Outline each Babesia divergens-infected red blood cell.
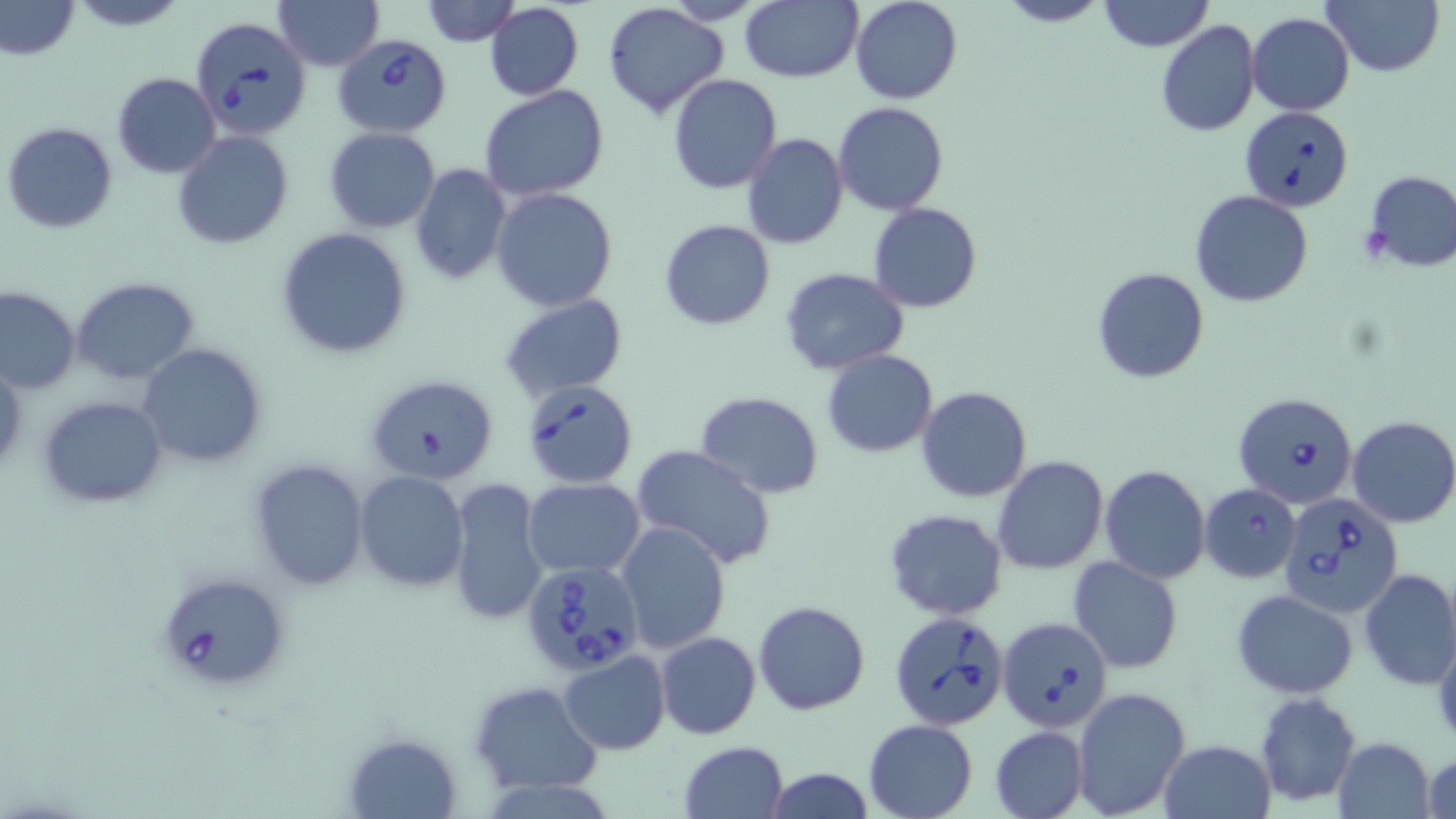

Approximate bounding boxes as [x1, y1, x2, y2] in pixels.
Babesia divergens-infected red blood cells: [189, 16, 312, 140], [333, 36, 454, 137], [1241, 105, 1354, 211], [519, 379, 640, 489], [1234, 392, 1359, 509], [1280, 490, 1404, 616], [520, 561, 645, 678], [154, 570, 292, 690], [889, 608, 1009, 727], [996, 615, 1112, 731].

slide-level diagnosis = Babesia divergens
magnification = 1000x
preparation = thin blood film
stain = May-Grünwald-Giemsa
modality = light microscopy
field of view = single
uninfected red blood cell locations = approximate bounding boxes as [x1, y1, x2, y2] in pixels: [2, 0, 78, 60], [67, 0, 187, 30], [272, 0, 384, 71], [421, 0, 520, 46], [739, 0, 862, 83], [849, 0, 963, 104], [995, 0, 1111, 27], [1098, 0, 1213, 53], [1322, 0, 1443, 76], [660, 1, 771, 24], [483, 2, 585, 100], [603, 3, 729, 117], [1247, 12, 1355, 115], [1156, 20, 1260, 136], [112, 73, 221, 178], [667, 73, 782, 193], [478, 86, 609, 202], [833, 101, 949, 215], [3, 122, 118, 234], [324, 127, 441, 233], [171, 130, 294, 249], [741, 133, 848, 252], [435, 146, 565, 281], [410, 164, 511, 285], [1361, 169, 1456, 272], [490, 188, 619, 312], [1190, 190, 1315, 308], [868, 202, 982, 313], [658, 218, 775, 331], [275, 228, 412, 359], [1091, 267, 1210, 384], [781, 268, 910, 375], [70, 277, 198, 386], [0, 286, 79, 394], [499, 294, 628, 404], [139, 343, 268, 468], [822, 349, 939, 458], [0, 361, 24, 479], [363, 372, 498, 485], [917, 385, 1032, 503], [693, 391, 824, 497], [38, 395, 167, 507], [1346, 416, 1456, 528], [631, 445, 777, 569], [992, 455, 1108, 574], [247, 457, 371, 592], [1100, 465, 1209, 583], [354, 472, 470, 592], [446, 477, 549, 627], [522, 478, 646, 578], [1199, 484, 1302, 583], [885, 509, 1008, 621], [615, 520, 732, 653], [1067, 557, 1184, 673], [1359, 568, 1456, 689], [1232, 589, 1359, 699], [753, 600, 869, 715], [655, 632, 762, 740], [558, 652, 670, 754], [467, 681, 604, 796], [1072, 688, 1190, 816], [1253, 691, 1362, 806], [861, 719, 980, 819], [990, 726, 1087, 818], [346, 735, 462, 817], [1335, 737, 1436, 819], [1158, 738, 1275, 818], [678, 741, 790, 819], [1422, 751, 1455, 819], [762, 766, 875, 819]
image size = 1456×819 pixels